Assess this cell for malaria.
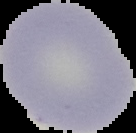
It is uninfected.

{
  "image_size": "136×133 pixels",
  "image_type": "segmented cell region on a black background",
  "preparation": "thin blood film"
}